Assess this cell for malaria.
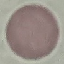

It is uninfected.

Summary:
  - Capture: smartphone through the microscope eyepiece
  - Stain: Giemsa
  - Image type: cell patch, automatically extracted from a larger field of view and resized to 64 × 64 pixels
  - Preparation: thin smear